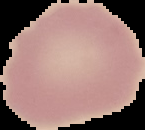 From a thin blood film. Image is 145×130 pixels. Malaria status: uninfected. Cell region segmented out of the field of view; the surrounding area is masked to black.